State which parasite is depicted.
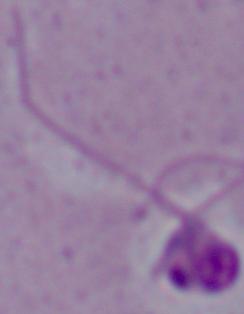

Leishmania.

magnification: 1000x
modality: micrograph